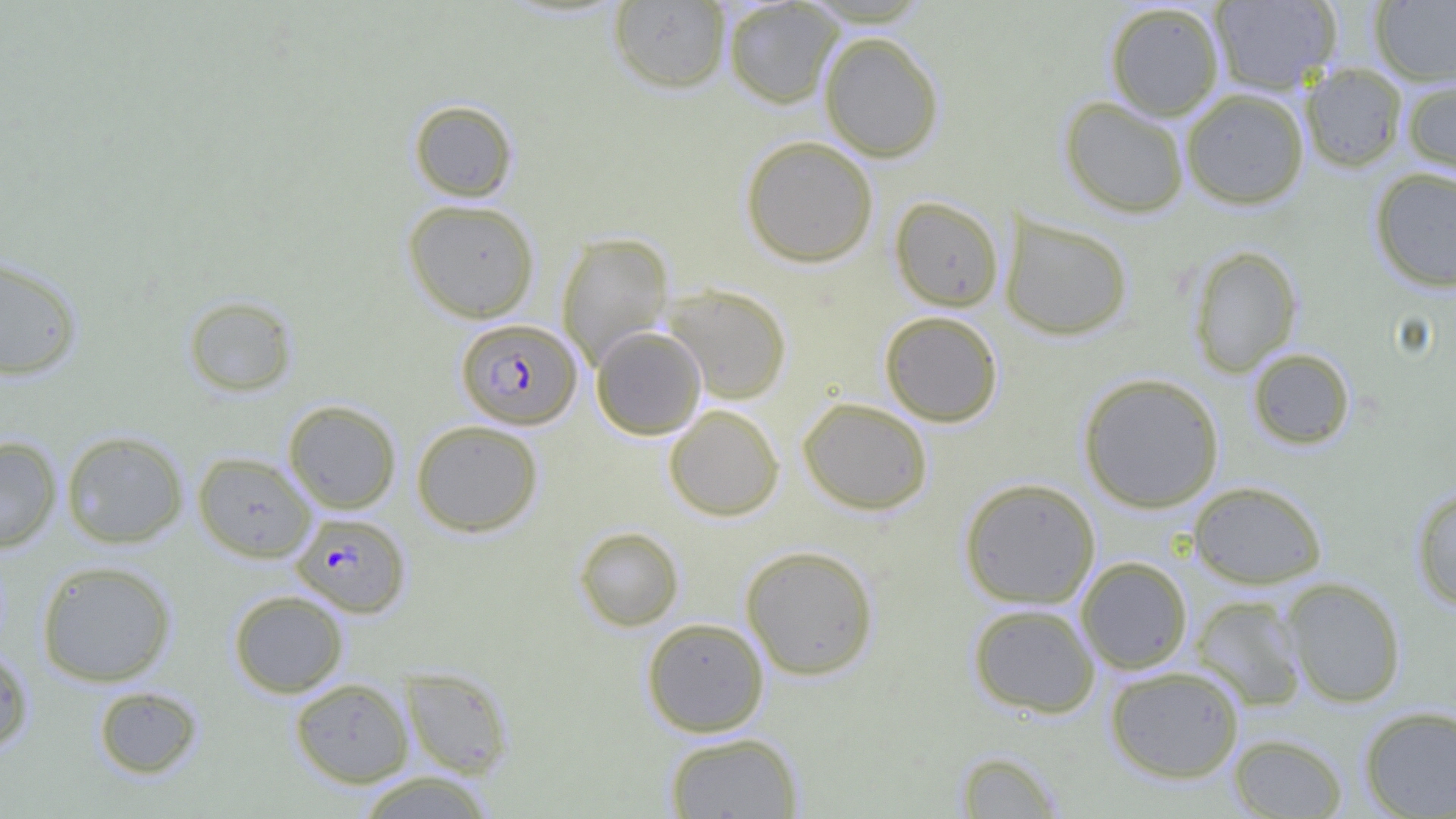
Summary:
  - Coordinate format: approximate bounding boxes as [x1, y1, x2, y2] in pixels
  - Uninfected red blood cell locations: [608, 1, 731, 94], [723, 1, 844, 109], [1209, 1, 1342, 95], [1370, 1, 1456, 86], [1104, 2, 1225, 120], [819, 31, 945, 162], [1300, 63, 1408, 173], [1401, 77, 1456, 181], [1180, 88, 1309, 209], [1059, 96, 1190, 218], [408, 100, 518, 202], [740, 135, 879, 267], [1369, 166, 1456, 292], [890, 196, 1004, 311], [402, 199, 540, 323], [999, 213, 1133, 341], [556, 231, 675, 368], [1187, 245, 1302, 377], [0, 255, 84, 380], [661, 283, 793, 405], [183, 294, 298, 397], [879, 311, 1004, 427], [591, 326, 706, 440], [1247, 347, 1355, 450], [1078, 373, 1224, 512], [797, 397, 933, 515], [283, 400, 401, 514], [664, 404, 784, 521], [411, 420, 543, 537], [61, 430, 188, 548], [0, 436, 62, 553], [193, 451, 316, 562], [959, 478, 1101, 609], [1188, 480, 1327, 589], [1411, 485, 1456, 611], [573, 526, 684, 631], [740, 544, 879, 681], [1076, 556, 1193, 674], [36, 560, 176, 686], [1281, 577, 1406, 708], [228, 590, 349, 698], [1190, 594, 1308, 711], [967, 603, 1100, 719], [641, 617, 770, 737], [0, 646, 35, 755], [1104, 665, 1246, 784], [400, 666, 514, 778], [290, 677, 414, 787], [93, 685, 204, 779], [1358, 705, 1456, 818], [664, 731, 804, 819], [1228, 734, 1348, 818], [953, 750, 1066, 818], [356, 771, 496, 818]
  - Plasmodium falciparum-infected red blood cell locations: [456, 318, 581, 429], [291, 512, 410, 617]
  - Slide-level diagnosis: Plasmodium falciparum
  - Magnification: 1000x
  - Field of view: one of a larger specimen
  - Image size: 1456×819 pixels
  - Preparation: thin blood film
  - Modality: optical microscopy